Give the position of every Plasmodium parasite visible.
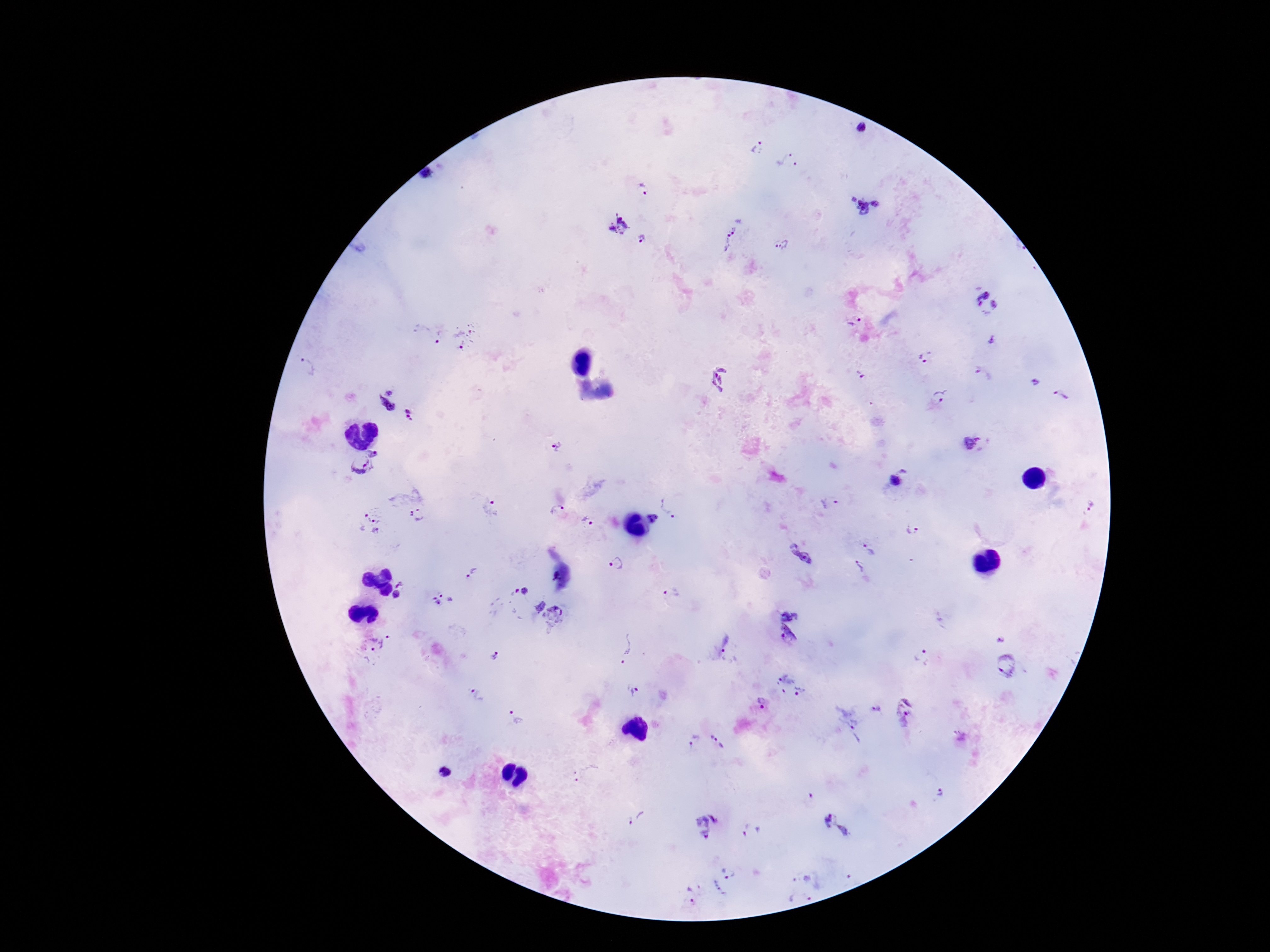
Approximate object centers, in pixels from the top-left corner.
Plasmodium parasites: (x=862, y=129), (x=758, y=149), (x=789, y=160), (x=643, y=190), (x=865, y=206), (x=619, y=225), (x=731, y=236), (x=642, y=237), (x=782, y=246), (x=987, y=302), (x=855, y=320), (x=430, y=334), (x=467, y=337), (x=924, y=358), (x=860, y=376), (x=720, y=379), (x=1034, y=382), (x=940, y=396), (x=1061, y=396), (x=390, y=400), (x=413, y=416), (x=972, y=441), (x=556, y=446), (x=374, y=451), (x=361, y=465), (x=899, y=477), (x=829, y=502), (x=671, y=504), (x=1091, y=505), (x=491, y=508), (x=558, y=510), (x=417, y=516), (x=654, y=518), (x=586, y=519), (x=371, y=524), (x=912, y=530), (x=870, y=550), (x=800, y=554), (x=617, y=564), (x=858, y=566), (x=473, y=573), (x=399, y=583), (x=673, y=592), (x=396, y=594), (x=519, y=596), (x=442, y=601), (x=538, y=605), (x=557, y=618), (x=788, y=631), (x=999, y=638), (x=375, y=647), (x=625, y=647), (x=722, y=647), (x=494, y=656), (x=922, y=657), (x=1004, y=664), (x=791, y=684), (x=633, y=689), (x=478, y=695), (x=762, y=704), (x=878, y=711), (x=904, y=712), (x=516, y=717), (x=852, y=732), (x=693, y=741), (x=717, y=742), (x=444, y=773), (x=588, y=774), (x=939, y=793), (x=637, y=818), (x=829, y=819), (x=707, y=825), (x=746, y=830), (x=844, y=831), (x=729, y=872), (x=718, y=890), (x=690, y=895).

Smartphone photograph taken through the microscope eyepiece. Patient malaria status: infected. Thick blood smear. 100x magnification. One field from this slide. Image is 1270×952 pixels. Giemsa stain.